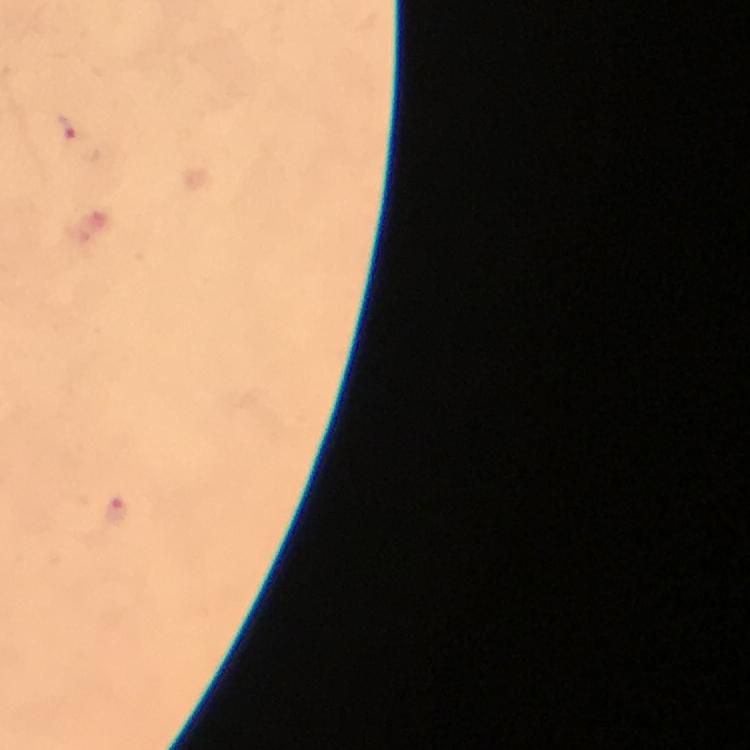

Approximate centers as [x, y] in pixels. Plasmodium parasite locations: [63, 129], [115, 509]. From a malaria diagnostic workup. Immersion oil was used. Image is 750×750 pixels. 100x magnification. Photographed with a smartphone mounted on the microscope. Thick smear. Giemsa stain. Cropped region of a single field of view.